Give the position of every malaria parasite, noting whether each is a trophozoite, schizont, or gametocyte.
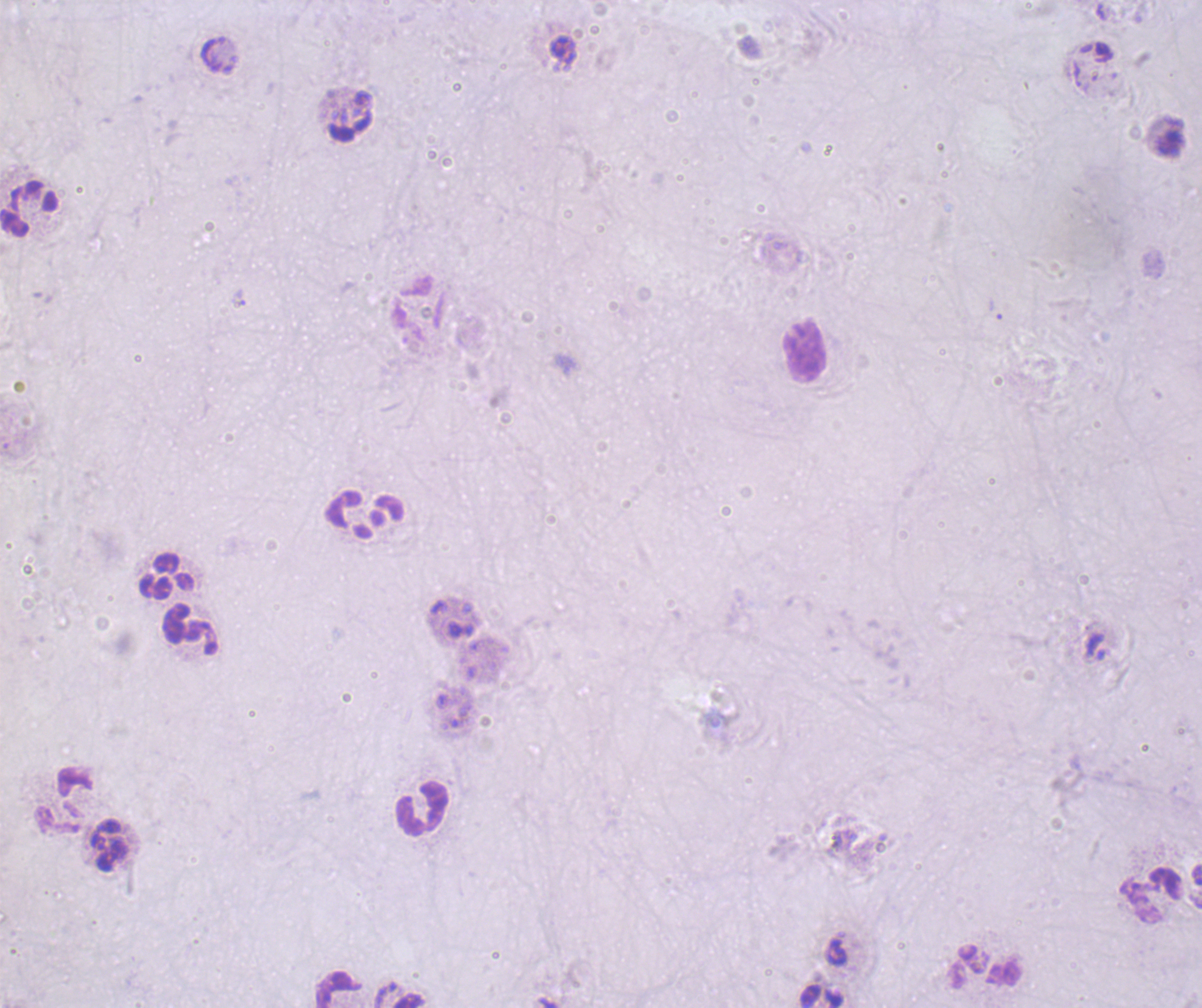
No malaria parasites detected.

context: previously used in an actual diagnosis
leukocyte_locations: 'approximate centers as {x, y} in pixels: {29, 208}, {804, 350}, {364, 515}, {165, 575}, {191, 631}, {62, 800}, {420, 808}, {108, 845}, {1150, 896}, {984, 966}, {337, 989}'
image_size: 1202×1008 pixels
coloration_quality: bad
preparation: thick blood smear
background_quality: poor
magnification: 100x
field_of_view: single
stain: Romanowsky